Point out each Plasmodium parasite.
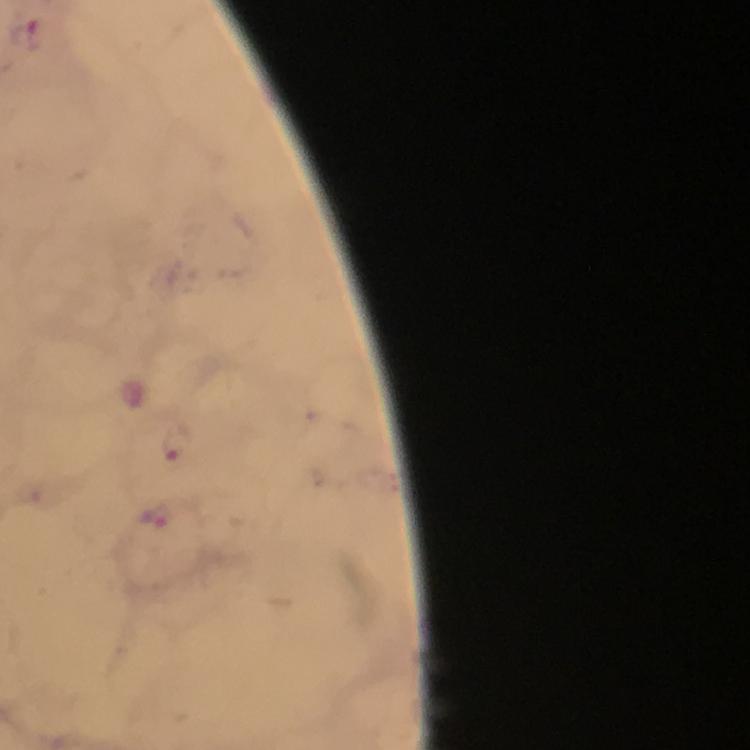
Approximate centers as (x, y) in pixels.
Plasmodium parasites: (174, 441), (158, 516).

cropped from = a single field of view
preparation = thick smear
capture = smartphone mounted on the microscope
stain = Giemsa
image size = 750×750 pixels
context = from a malaria diagnostic workup
magnification = 100x
immersion oil = applied